Describe the morphology of the erythrocytes.
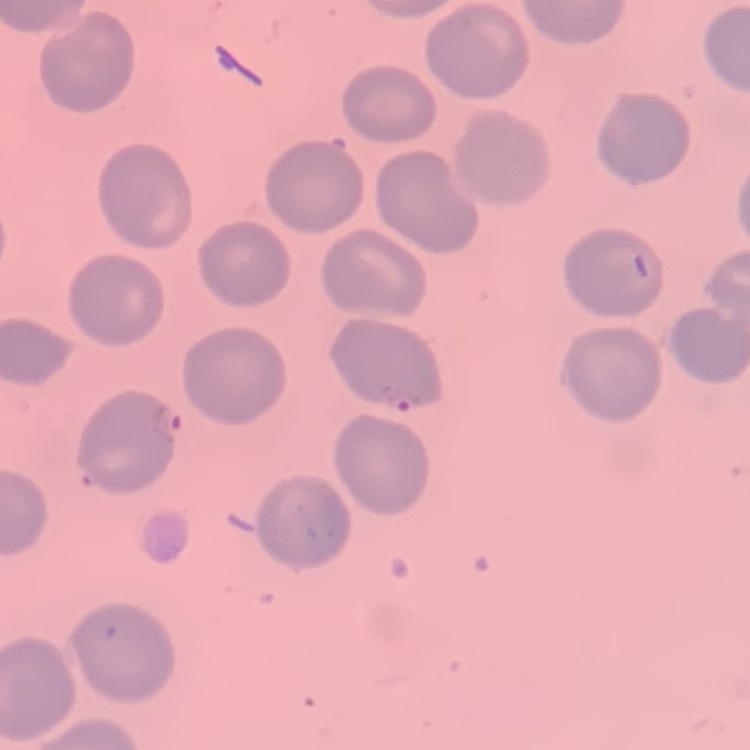
No rouleaux formation.

Stained with either Field's or Giemsa. Square crop of a larger photomicrograph. Thin peripheral smear.